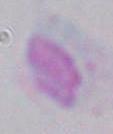
Summary:
  - Identification: Toxoplasma gondii
  - Magnification: 1000x
  - Modality: micrograph